Describe the morphology of the erythrocytes.
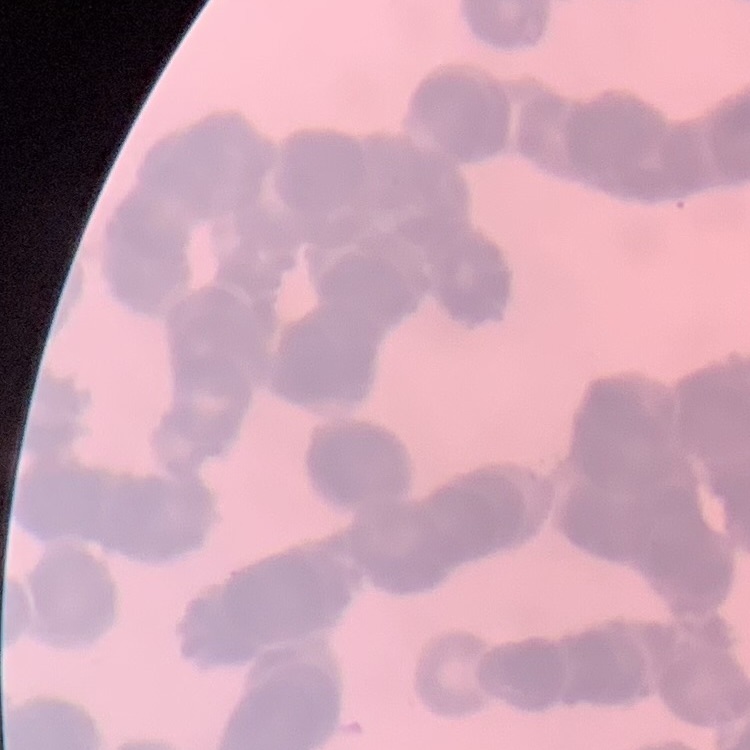
They show rouleaux formation.

preparation: thin peripheral smear
image_type: square crop of a larger photomicrograph
stain: Field's or Giemsa